Assess the morphology of the erythrocytes.
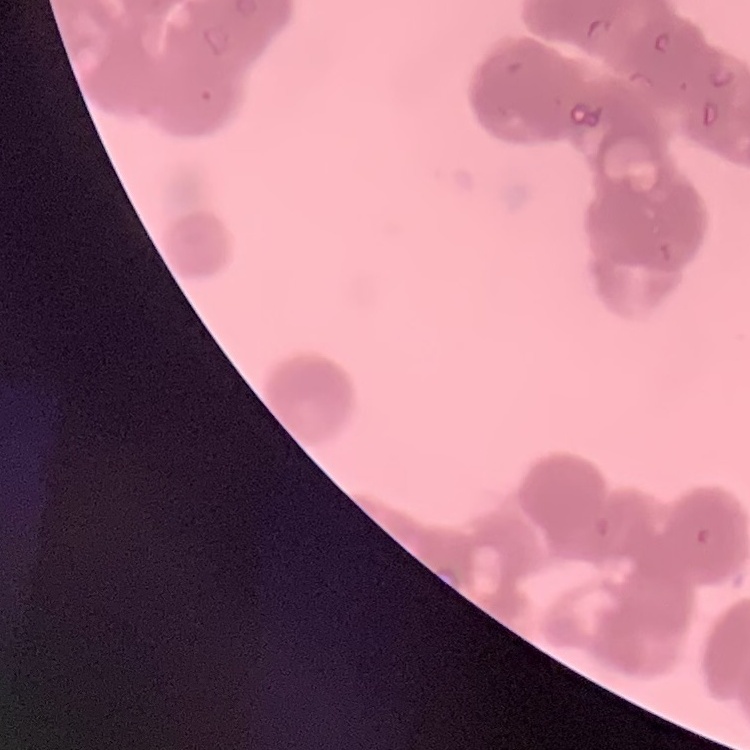
They show rouleaux formation.

Thin blood film. One tile cut from a larger photomicrograph. Stained with either Field's or Giemsa.